Give the extent of all Plasmodium falciparum-infected red blood cells.
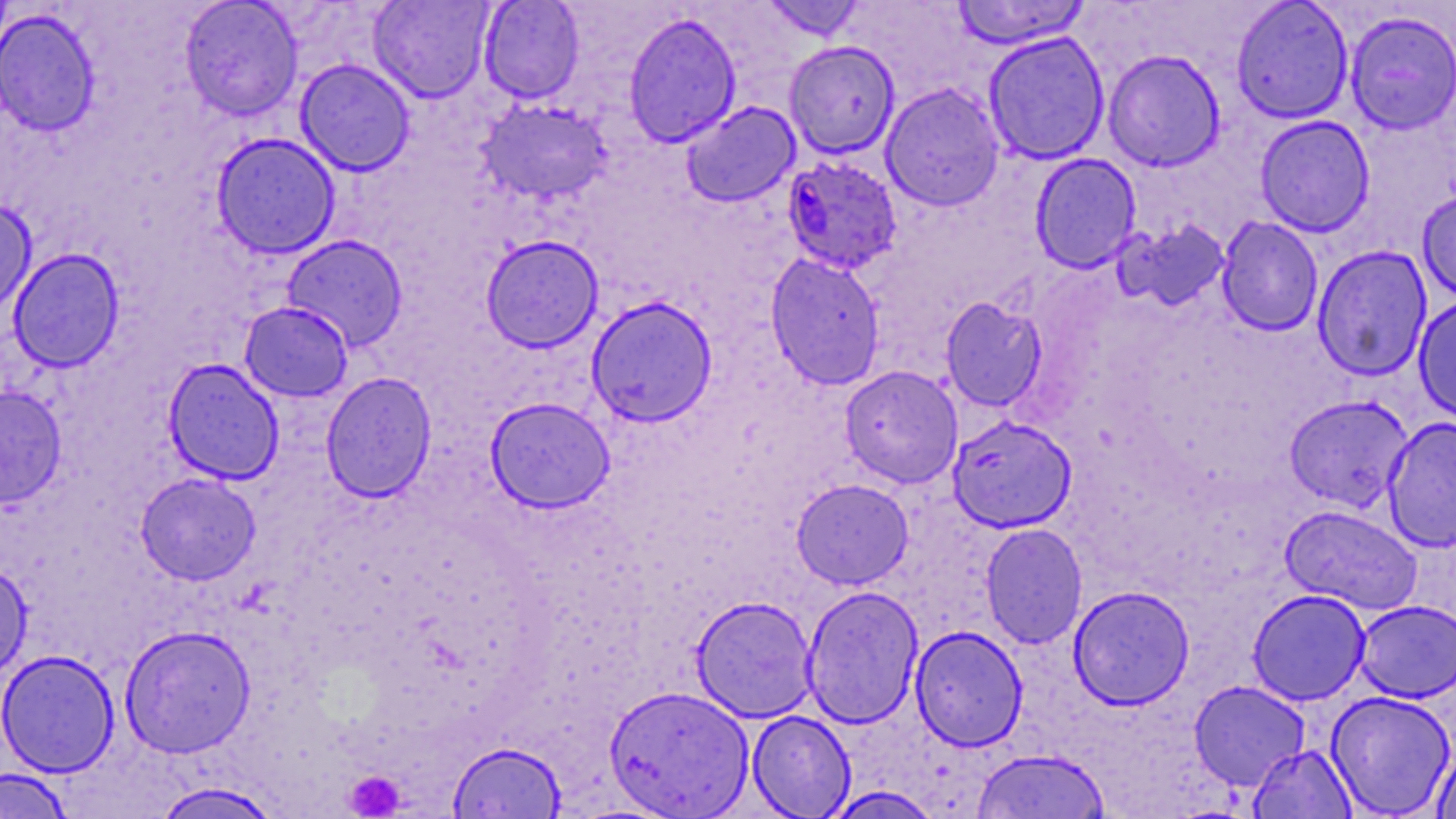
Approximate bounding boxes as (x1,y1)-(x2,y2) corner pairs in pixels.
Plasmodium falciparum-infected red blood cells: (781,155)-(902,274).

Platelet locations: (344,770)-(405,817). Uninfected red blood cell locations: (0,0)-(13,55), (179,0)-(304,121), (368,0)-(495,103), (478,0)-(585,104), (760,0)-(867,41), (950,0)-(1091,49), (1231,0)-(1354,124), (0,8)-(101,137), (1344,10)-(1456,135), (623,11)-(742,149), (983,31)-(1110,165), (784,40)-(900,159), (1103,49)-(1226,172), (294,59)-(416,177), (881,82)-(1004,212), (475,99)-(612,204), (680,101)-(801,208), (1254,115)-(1376,237), (210,132)-(341,259), (1030,153)-(1141,273), (1417,187)-(1456,305), (0,200)-(37,316), (1216,216)-(1323,337), (1112,219)-(1231,314), (281,234)-(409,352), (480,234)-(604,353), (1312,245)-(1433,382), (7,248)-(125,372), (765,252)-(886,391), (586,295)-(718,427), (1412,295)-(1456,424), (940,297)-(1048,411), (239,301)-(353,402), (163,358)-(285,485), (840,365)-(963,488), (320,371)-(438,503), (0,384)-(67,509), (1284,394)-(1413,513), (485,397)-(615,513), (947,415)-(1077,533), (1382,416)-(1456,553), (135,472)-(261,585), (791,478)-(914,589), (1280,504)-(1422,615), (980,522)-(1087,650), (0,562)-(33,682), (801,585)-(924,729), (1068,585)-(1194,710), (1247,589)-(1371,705), (690,595)-(818,723), (1354,599)-(1456,703), (119,624)-(256,758), (910,626)-(1029,751), (0,649)-(120,777), (1188,680)-(1311,790), (604,685)-(754,818), (1326,690)-(1456,817), (746,710)-(856,818), (447,740)-(567,819), (1432,741)-(1456,819), (1248,744)-(1357,818), (971,748)-(1111,819), (0,768)-(75,818), (150,782)-(284,819), (823,786)-(944,818). Slide-level diagnosis: Plasmodium falciparum. Optical microscopy. One field of a larger specimen. May-Grünwald-Giemsa stain. 1000x magnification. Thin blood smear. Image is 1456×819 pixels.